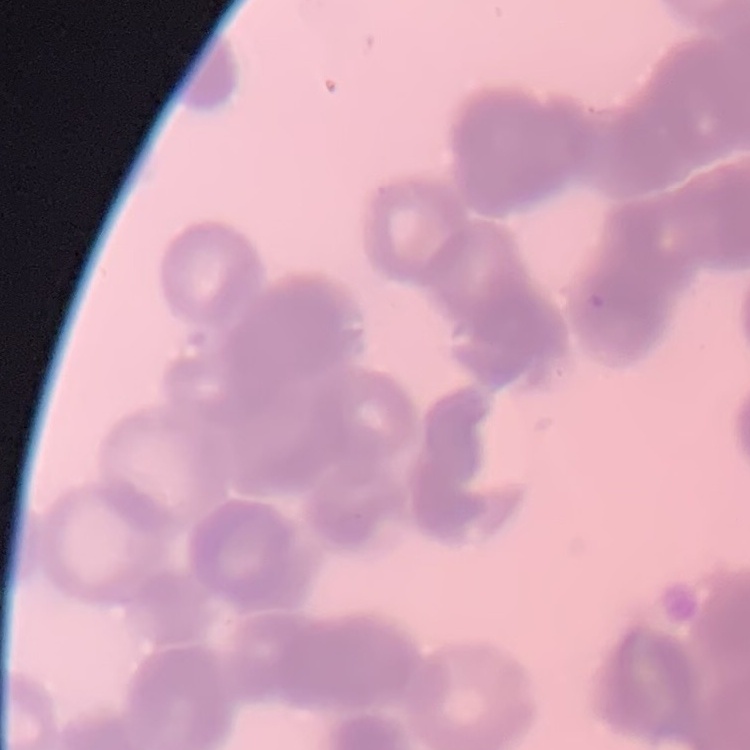

erythrocyte morphology = rouleaux formation
image type = square crop of a larger photomicrograph
preparation = thin blood smear
stain = Field's or Giemsa